Assess this cell for malaria.
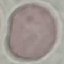
It is uninfected.

preparation: thin blood smear
image_type: cell patch, automatically extracted from a larger field of view and resized to 64 × 64 pixels
stain: Giemsa
capture: smartphone camera at the microscope eyepiece